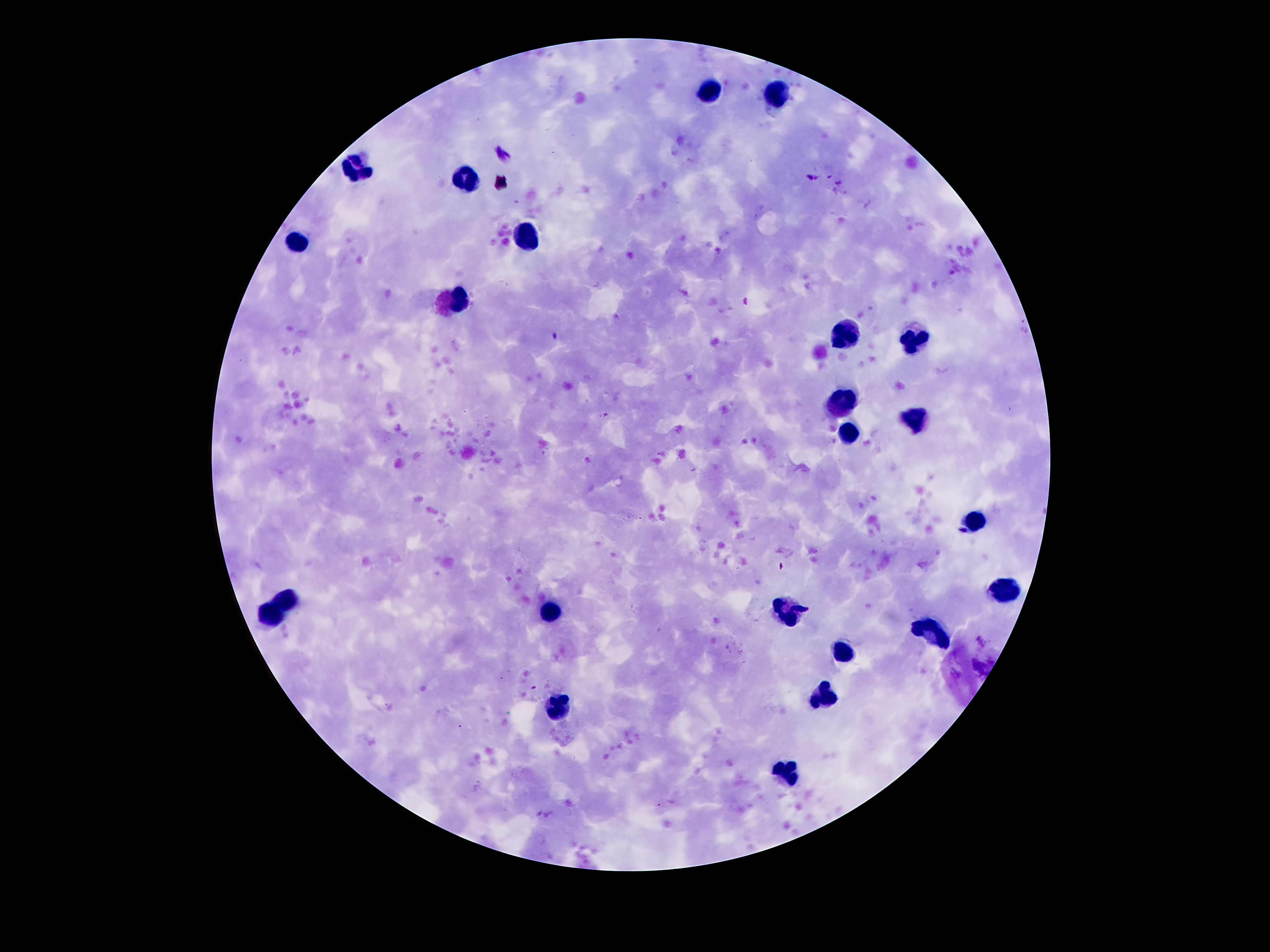
Approximate centers as {x, y} in pixels. Leukocyte locations: {707, 90}, {780, 95}, {353, 169}, {465, 179}, {297, 242}, {526, 242}, {452, 305}, {849, 337}, {912, 339}, {843, 400}, {914, 423}, {846, 431}, {977, 520}, {1004, 589}, {287, 599}, {271, 612}, {791, 612}, {549, 615}, {933, 628}, {843, 649}, {825, 696}, {560, 707}, {786, 772}. Thick blood film. 100x magnification. Patient malaria status: negative. Image is 1270×952 pixels. Smartphone photograph taken through the microscope eyepiece. Single field of view. Giemsa stain.